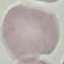

Result: negative for malaria parasites. Thin blood film. Automatically extracted cell patch, resized to 64 × 64 pixels. Giemsa-stained preparation. Photographed with a smartphone camera at the microscope eyepiece.